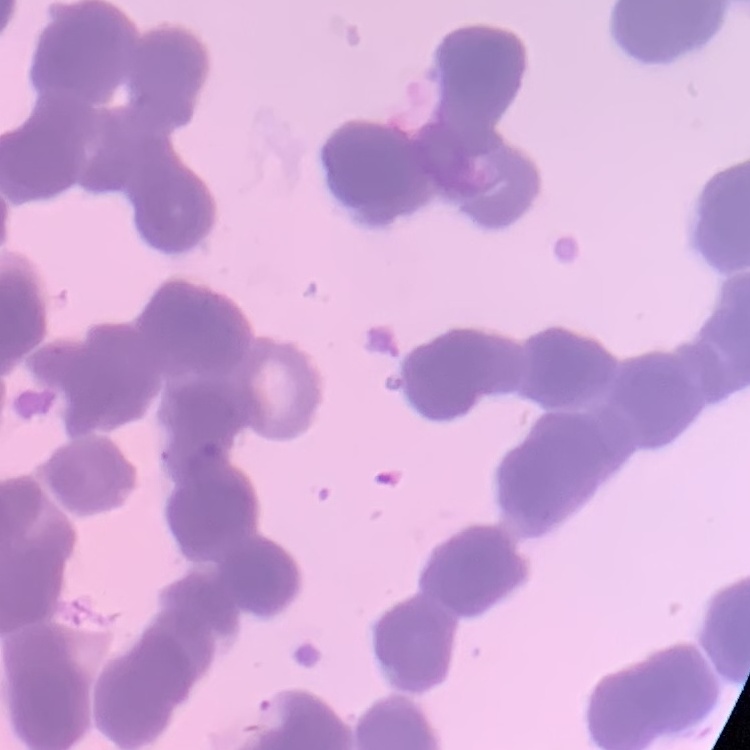

The red blood cells show rouleaux formation. Thin blood smear. Stained with either Field's or Giemsa. Square crop of a larger photomicrograph.